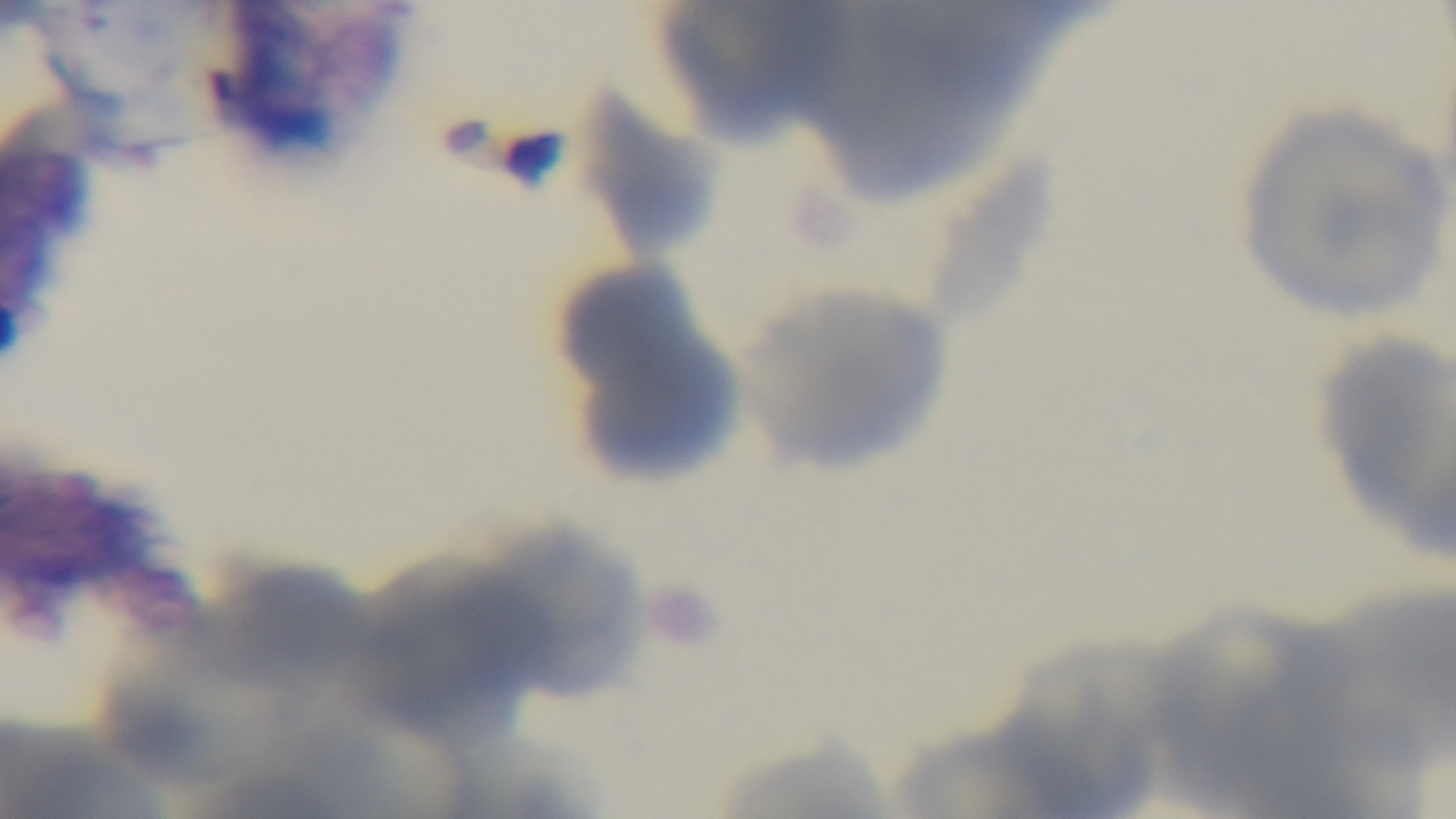
stain: Giemsa
preparation: thin smear
modality: light microscopy
capture: mounted 4K digital camera
field_of_view: single
malaria_status: uninfected
objective: 100x oil immersion